Classify this cell by malaria status.
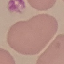

Uninfected.

Acquired by smartphone through the microscope eyepiece. Automatically extracted cell patch, resized to 64 × 64 pixels. Thin blood smear. Giemsa-stained preparation.